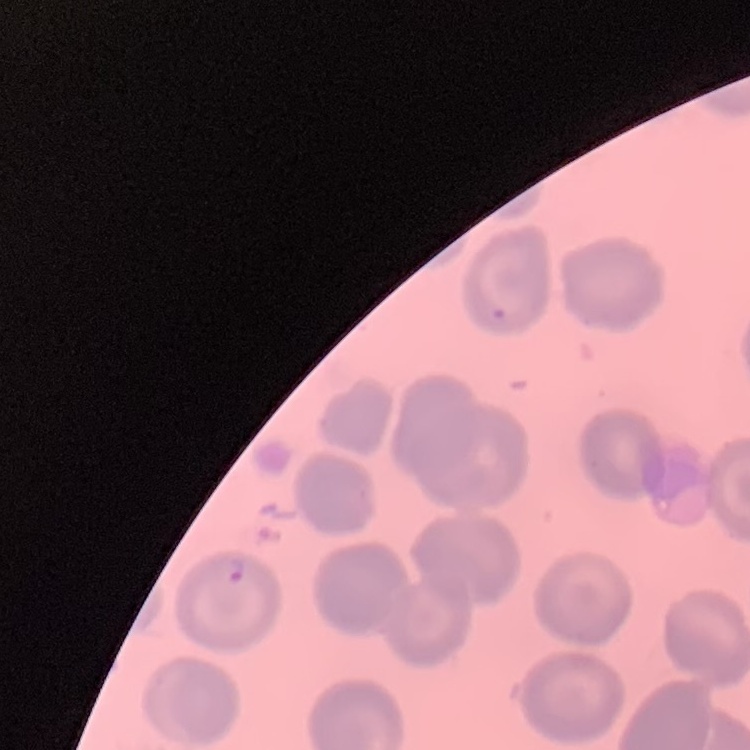

Summary:
  - Erythrocyte morphology: no rouleaux formation
  - Image type: one tile cut from a larger photomicrograph
  - Stain: Field's or Giemsa
  - Preparation: thin peripheral smear